Identify the blood parasite species.
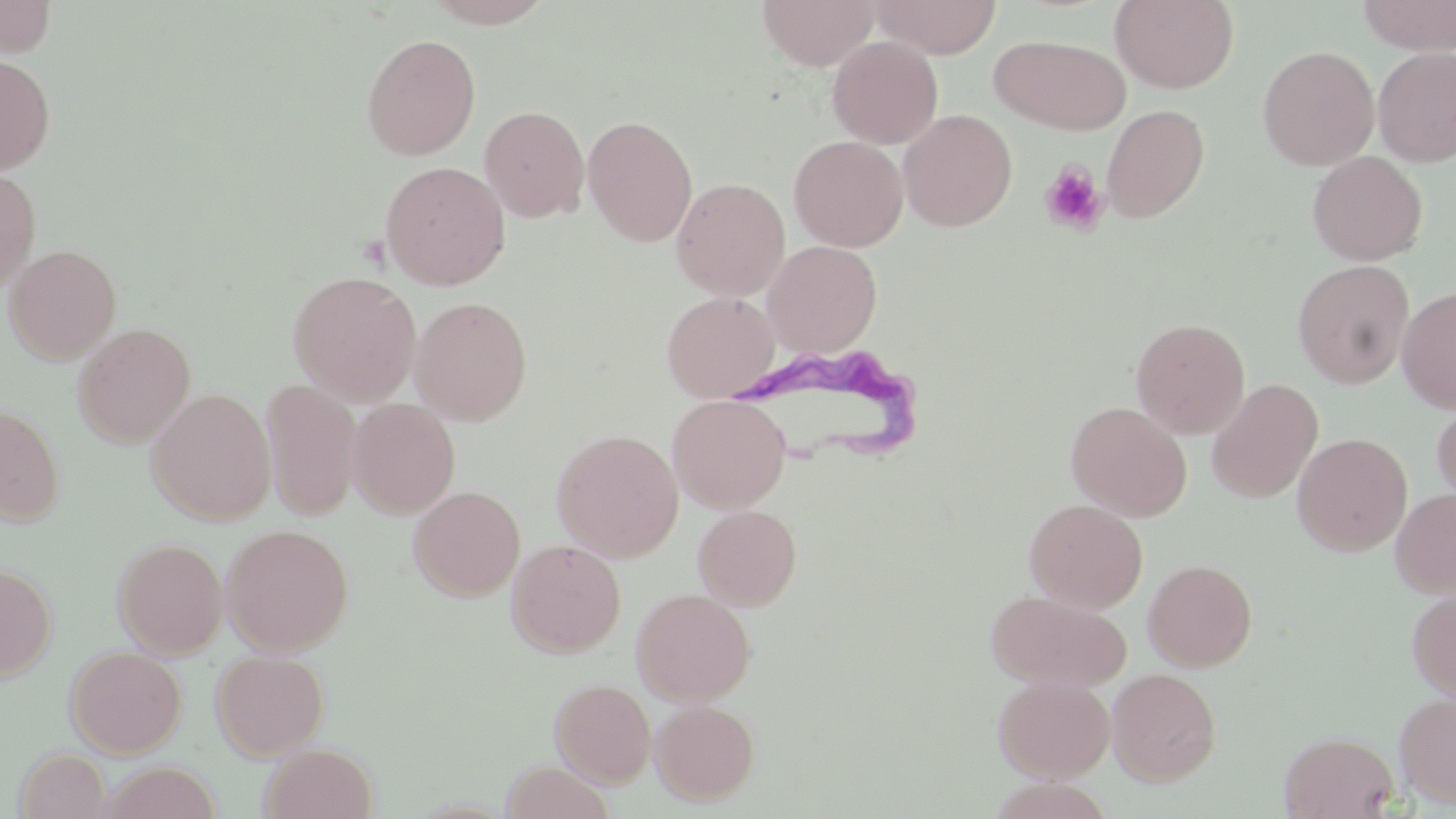
Trypanosoma brucei.

Approximate bounding boxes as named x1/y1/x2/y2 corners in pixels. Uninfected red blood cell locations: (x1=0, y1=0, x2=58, y2=58), (x1=421, y1=0, x2=558, y2=28), (x1=756, y1=0, x2=880, y2=70), (x1=868, y1=0, x2=1001, y2=58), (x1=1110, y1=0, x2=1239, y2=92), (x1=1356, y1=0, x2=1455, y2=55), (x1=361, y1=33, x2=481, y2=161), (x1=990, y1=34, x2=1131, y2=135), (x1=827, y1=35, x2=943, y2=149), (x1=1257, y1=45, x2=1379, y2=170), (x1=1373, y1=47, x2=1456, y2=167), (x1=0, y1=54, x2=56, y2=174), (x1=1101, y1=104, x2=1210, y2=223), (x1=479, y1=105, x2=590, y2=223), (x1=898, y1=109, x2=1017, y2=231), (x1=583, y1=114, x2=698, y2=247), (x1=788, y1=135, x2=908, y2=252), (x1=1307, y1=151, x2=1428, y2=266), (x1=380, y1=161, x2=510, y2=291), (x1=0, y1=167, x2=41, y2=295), (x1=671, y1=177, x2=791, y2=300), (x1=762, y1=240, x2=882, y2=357), (x1=4, y1=244, x2=122, y2=364), (x1=1292, y1=260, x2=1414, y2=388), (x1=287, y1=270, x2=422, y2=405), (x1=1396, y1=287, x2=1456, y2=414), (x1=661, y1=291, x2=780, y2=402), (x1=410, y1=296, x2=532, y2=425), (x1=1130, y1=317, x2=1251, y2=439), (x1=72, y1=323, x2=195, y2=448), (x1=261, y1=379, x2=363, y2=522), (x1=1207, y1=379, x2=1324, y2=503), (x1=146, y1=389, x2=276, y2=525), (x1=667, y1=394, x2=791, y2=513), (x1=1431, y1=396, x2=1456, y2=512), (x1=346, y1=398, x2=461, y2=518), (x1=1065, y1=401, x2=1193, y2=521), (x1=0, y1=404, x2=65, y2=527), (x1=551, y1=428, x2=684, y2=562), (x1=1292, y1=433, x2=1413, y2=556), (x1=409, y1=485, x2=525, y2=601), (x1=1390, y1=488, x2=1456, y2=597), (x1=1024, y1=499, x2=1148, y2=613), (x1=693, y1=505, x2=802, y2=610), (x1=220, y1=523, x2=354, y2=656), (x1=112, y1=536, x2=228, y2=658), (x1=506, y1=539, x2=626, y2=658), (x1=1142, y1=558, x2=1258, y2=671), (x1=0, y1=563, x2=57, y2=683), (x1=1406, y1=586, x2=1456, y2=705), (x1=631, y1=588, x2=755, y2=706), (x1=986, y1=589, x2=1131, y2=692), (x1=65, y1=646, x2=186, y2=758), (x1=210, y1=649, x2=329, y2=760), (x1=1107, y1=667, x2=1222, y2=786), (x1=992, y1=674, x2=1115, y2=782), (x1=550, y1=678, x2=656, y2=787), (x1=1394, y1=690, x2=1456, y2=809), (x1=650, y1=699, x2=760, y2=806), (x1=1279, y1=730, x2=1399, y2=818), (x1=260, y1=743, x2=378, y2=819), (x1=14, y1=748, x2=110, y2=818), (x1=500, y1=761, x2=615, y2=819), (x1=99, y1=762, x2=224, y2=818). Platelet locations: (x1=1039, y1=161, x2=1109, y2=237). Trypanosoma brucei locations: (x1=740, y1=352, x2=922, y2=477). Image is 1456×819 pixels. Single field of view. Thin blood film. Captured at 1000x magnification. May-Grünwald-Giemsa-stained preparation. Optical microscopy.